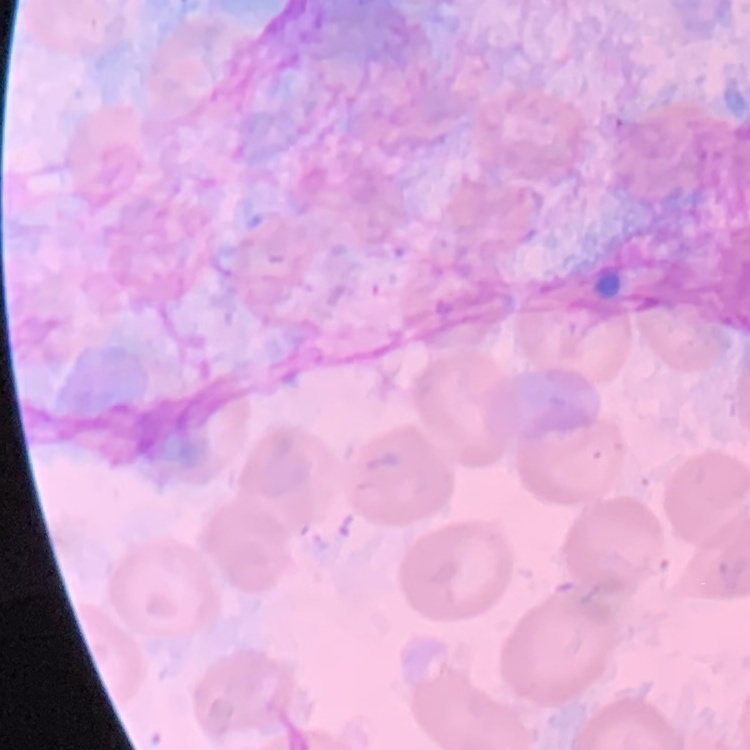
Summary:
  - Red blood cell morphology: no rouleaux formation
  - Preparation: thin peripheral smear
  - Image type: square crop of a larger photomicrograph
  - Stain: Field's or Giemsa